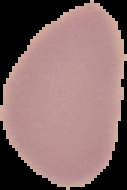
result: no Plasmodium parasites seen
preparation: thin blood smear
image_size: 127×190 pixels
image_type: segmented cell region on a black background